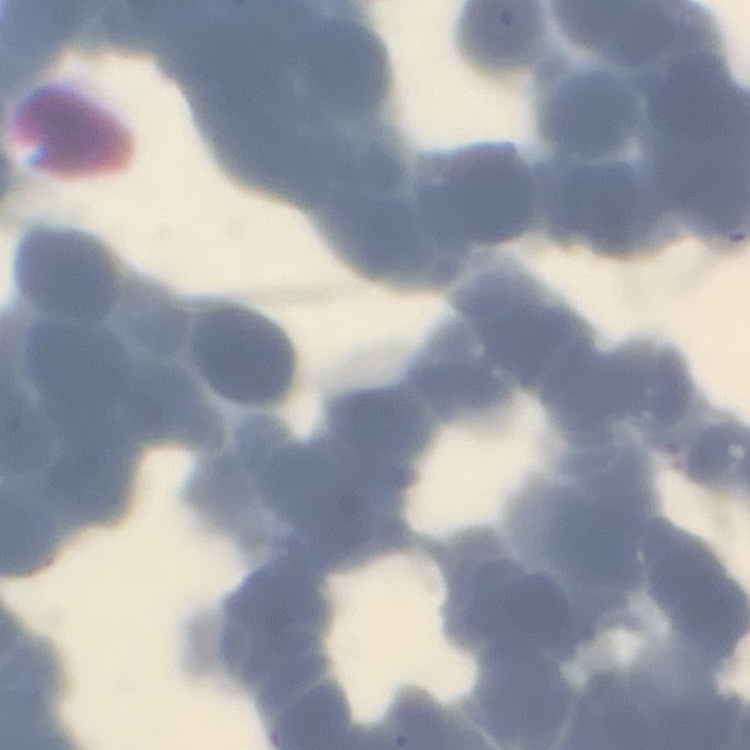 The erythrocytes exhibit rouleaux formation. Square crop of a larger photomicrograph. Field's or Giemsa stain. Thin peripheral smear.